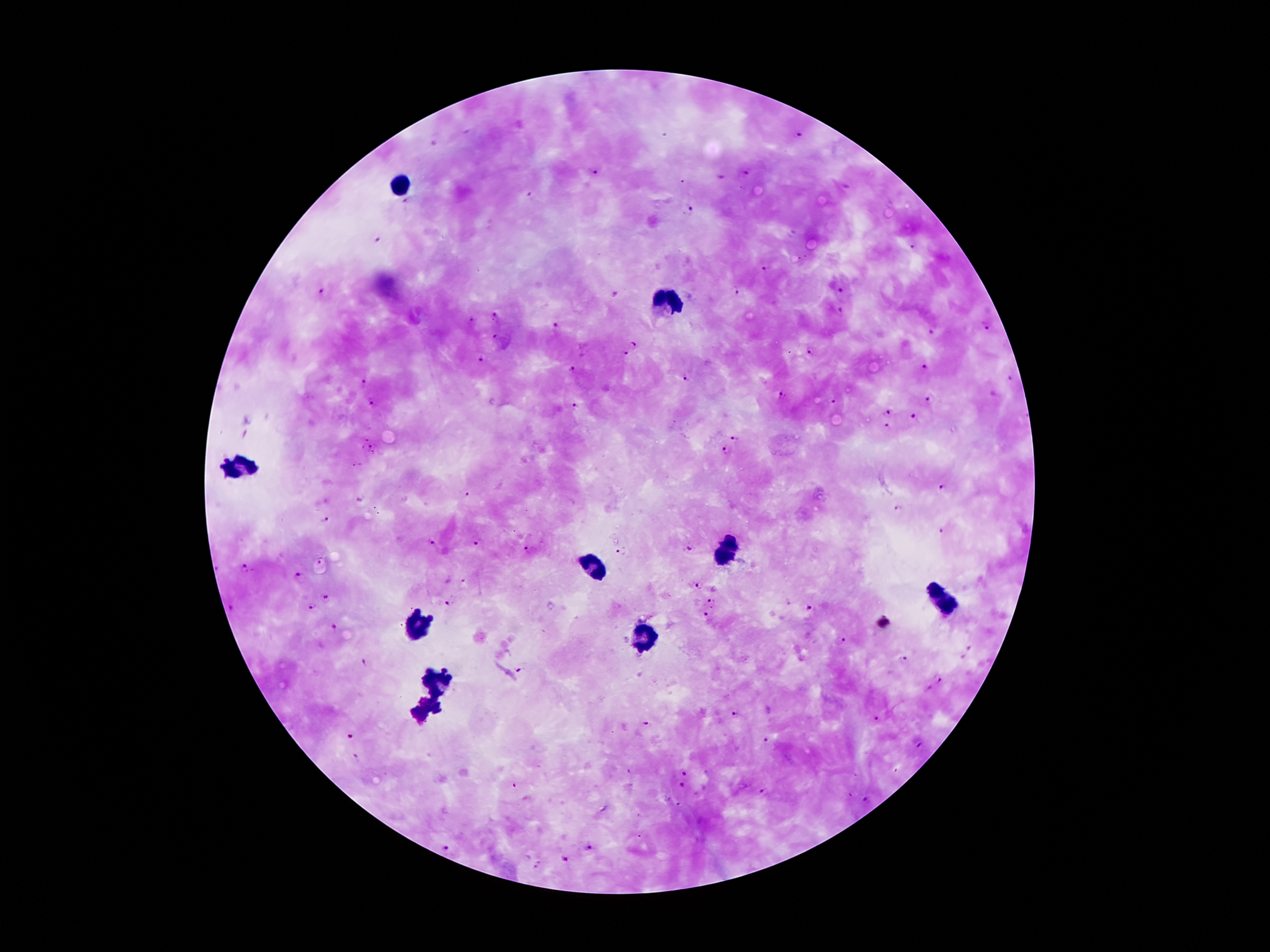
Approximate object centers, in pixels from the top-left corner. Malaria parasite locations: (x=468, y=132), (x=801, y=135), (x=595, y=171), (x=747, y=174), (x=719, y=176), (x=848, y=188), (x=531, y=194), (x=688, y=210), (x=377, y=240), (x=911, y=247), (x=764, y=268), (x=735, y=290), (x=321, y=292), (x=838, y=292), (x=614, y=295), (x=839, y=312), (x=497, y=317), (x=474, y=322), (x=986, y=325), (x=555, y=328), (x=932, y=332), (x=497, y=338), (x=633, y=344), (x=810, y=352), (x=626, y=354), (x=481, y=359), (x=925, y=367), (x=572, y=368), (x=687, y=377), (x=1010, y=379), (x=364, y=383), (x=992, y=394), (x=782, y=396), (x=928, y=398), (x=833, y=401), (x=372, y=404), (x=574, y=405), (x=886, y=412), (x=916, y=418), (x=888, y=426), (x=732, y=436), (x=374, y=447), (x=721, y=452), (x=943, y=488), (x=466, y=495), (x=897, y=510), (x=325, y=519), (x=943, y=532), (x=479, y=543), (x=434, y=544), (x=690, y=548), (x=527, y=551), (x=618, y=553), (x=245, y=570), (x=300, y=577), (x=465, y=582), (x=699, y=586), (x=327, y=597), (x=711, y=603), (x=448, y=604), (x=231, y=605), (x=311, y=607), (x=810, y=609), (x=706, y=614), (x=333, y=627), (x=840, y=640), (x=903, y=660), (x=364, y=663), (x=520, y=670), (x=938, y=679), (x=734, y=714), (x=879, y=717), (x=645, y=725), (x=350, y=735), (x=764, y=741), (x=919, y=745), (x=357, y=757), (x=685, y=772), (x=681, y=787), (x=767, y=790), (x=668, y=799), (x=866, y=800), (x=679, y=806), (x=589, y=846), (x=446, y=847), (x=564, y=859), (x=537, y=864). Leukocyte locations: (x=402, y=185), (x=669, y=302), (x=241, y=466), (x=726, y=552), (x=596, y=569), (x=948, y=602), (x=419, y=623), (x=419, y=625), (x=644, y=632), (x=438, y=678), (x=428, y=709). Image is 1270×952 pixels. Single field of view. 100x magnification. Giemsa-stained preparation. Patient malaria status: positive for Plasmodium falciparum. Photographed through the microscope eyepiece with a smartphone camera. Thick peripheral-blood smear.